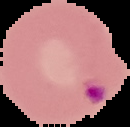 From a thin blood film. Image is 130×127 pixels. Cell region segmented out of the field of view; the surrounding area is masked to black. Malaria status: parasitized.